Name the parasite shown.
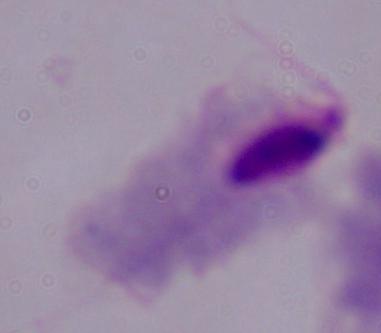
This is a trichomonad.

modality = photomicrograph
magnification = 1000x